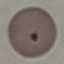
Malaria status: uninfected. Acquired by smartphone through the microscope eyepiece. Giemsa stain. Automatically extracted cell patch, resized to 64 × 64 pixels. Thin blood film.